Name the parasite shown.
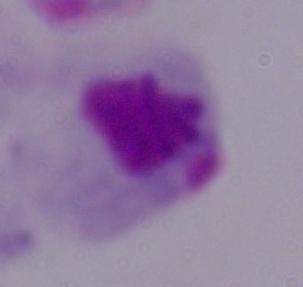

A trichomonad.

modality = micrograph
magnification = 1000x